State which cell type is depicted.
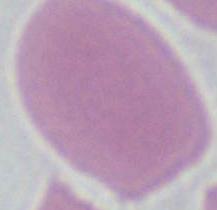
An erythrocyte.

modality: micrograph
magnification: 1000x